Locate every malaria parasite.
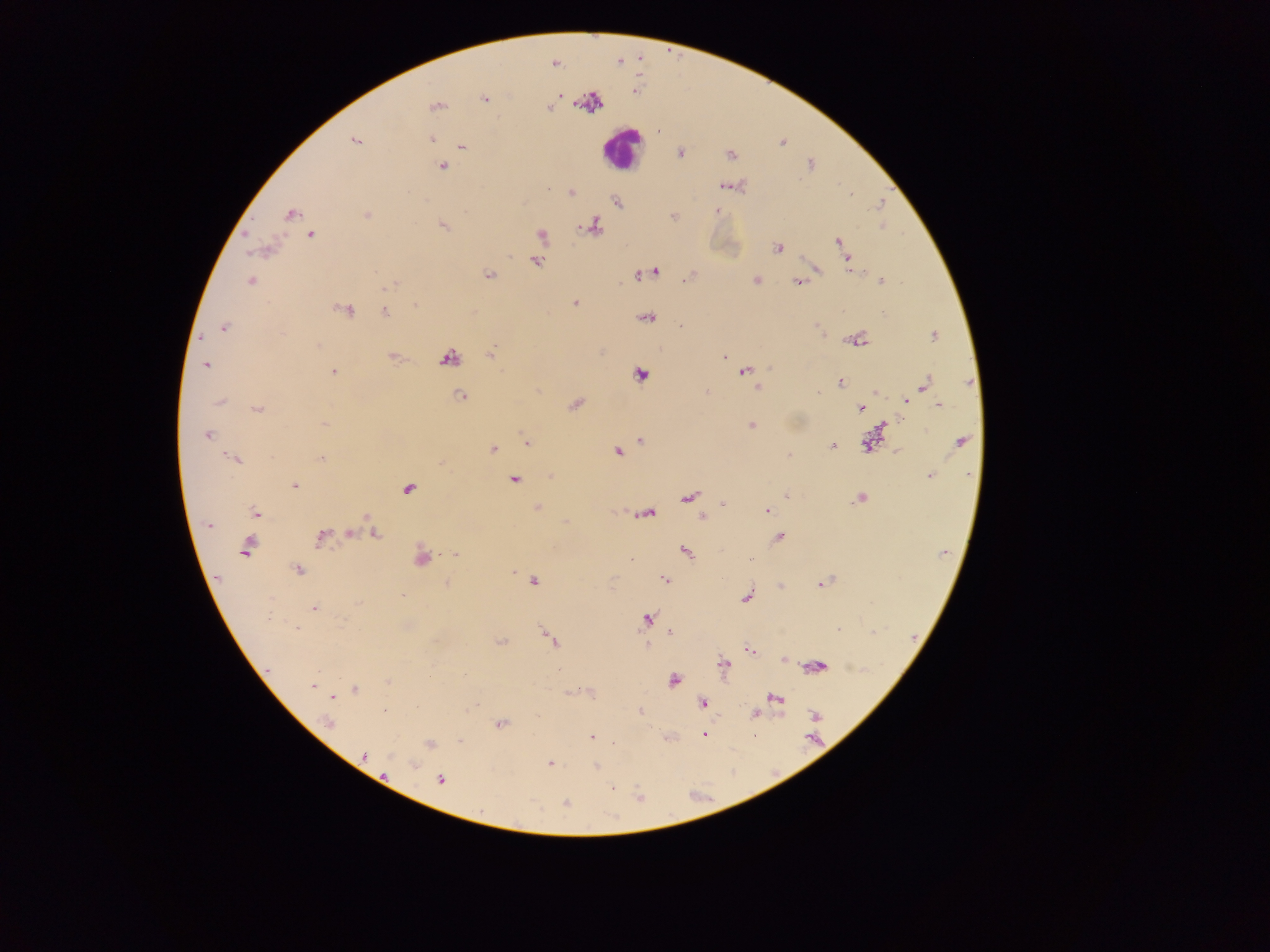
Approximate centers as {x, y} in pixels.
Malaria parasites: {554, 64}, {560, 96}, {485, 98}, {436, 106}, {550, 107}, {431, 139}, {355, 141}, {463, 146}, {679, 153}, {730, 155}, {442, 167}, {723, 186}, {572, 193}, {853, 193}, {617, 202}, {292, 214}, {367, 215}, {442, 225}, {593, 227}, {542, 235}, {312, 236}, {837, 241}, {777, 247}, {536, 262}, {849, 264}, {817, 269}, {851, 269}, {654, 272}, {640, 274}, {488, 275}, {687, 278}, {756, 280}, {881, 280}, {251, 282}, {798, 282}, {392, 285}, {574, 303}, {416, 306}, {347, 310}, {385, 311}, {647, 318}, {680, 326}, {223, 327}, {934, 335}, {858, 339}, {490, 354}, {392, 356}, {724, 356}, {448, 357}, {729, 364}, {206, 365}, {744, 371}, {333, 372}, {640, 375}, {840, 383}, {926, 384}, {758, 387}, {876, 392}, {707, 393}, {818, 393}, {461, 396}, {907, 401}, {220, 402}, {575, 404}, {939, 405}, {860, 407}, {257, 410}, {324, 424}, {884, 424}, {751, 426}, {207, 435}, {640, 440}, {962, 441}, {526, 443}, {868, 445}, {832, 446}, {493, 449}, {617, 451}, {787, 455}, {321, 458}, {234, 459}, {929, 475}, {514, 481}, {295, 486}, {408, 489}, {786, 495}, {688, 498}, {860, 498}, {723, 504}, {536, 507}, {767, 510}, {255, 513}, {649, 514}, {701, 516}, {369, 519}, {209, 524}, {350, 533}, {376, 533}, {321, 536}, {778, 537}, {246, 548}, {686, 553}, {456, 555}, {422, 559}, {630, 559}, {752, 559}, {298, 570}, {513, 572}, {664, 579}, {534, 581}, {447, 584}, {822, 584}, {781, 586}, {403, 596}, {746, 597}, {358, 603}, {313, 608}, {646, 620}, {296, 628}, {839, 629}, {672, 633}, {552, 640}, {501, 641}, {749, 650}, {784, 660}, {724, 665}, {817, 666}, {673, 680}, {388, 682}, {312, 686}, {355, 690}, {775, 698}, {702, 702}, {417, 707}, {640, 711}, {384, 712}, {756, 713}, {814, 715}, {329, 723}, {501, 724}, {703, 734}, {591, 737}, {459, 741}, {614, 743}, {429, 744}, {365, 755}, {549, 763}, {413, 764}, {596, 767}, {441, 780}, {612, 787}, {640, 796}, {566, 802}.

Leukocyte locations: {621, 148}. Image is 1270×952 pixels. One field of view. Sample from Ghana. Mobile-phone photograph taken through the microscope. Thick blood film.